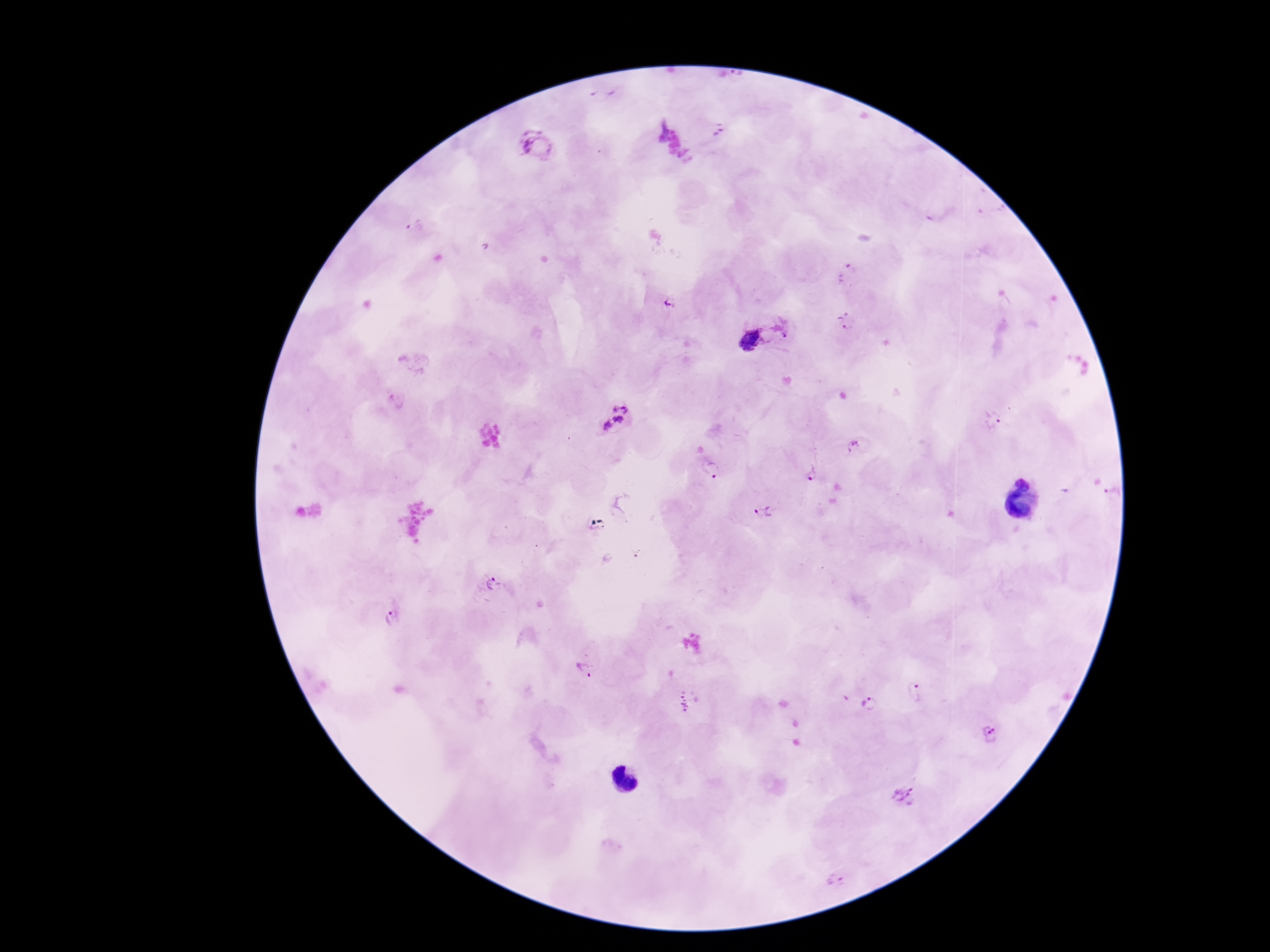
Approximate object centers, in pixels from the top-left corner. Plasmodium parasite locations: (x=658, y=130), (x=719, y=131), (x=535, y=145), (x=416, y=226), (x=671, y=304), (x=846, y=322), (x=751, y=340), (x=614, y=418), (x=994, y=420), (x=852, y=446), (x=713, y=470), (x=812, y=473), (x=1025, y=478), (x=1113, y=491), (x=763, y=512), (x=494, y=585), (x=394, y=619), (x=585, y=672), (x=914, y=692), (x=869, y=703), (x=691, y=704), (x=991, y=734), (x=904, y=796), (x=836, y=881). 100x magnification. Photographed through the microscope eyepiece with a smartphone camera. One field from this slide. Image is 1270×952 pixels. Giemsa-stained preparation. Patient malaria status: infected. Thick peripheral-blood smear.